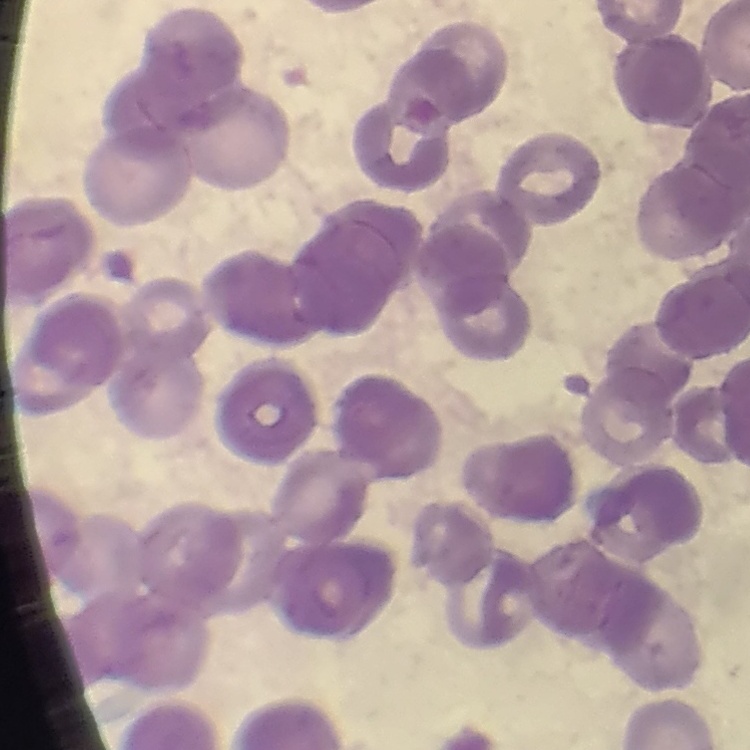

erythrocyte_morphology: rouleaux formation
image_type: one tile cut from a larger photomicrograph
stain: Field's or Giemsa
preparation: thin peripheral smear